Classify this cell by malaria status.
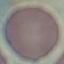

It is uninfected.

Thin blood smear. Giemsa-stained preparation. Cell patch, automatically extracted from a larger field of view and resized to 64 × 64 pixels. Photographed with a smartphone camera at the microscope eyepiece.